Describe the morphology of the erythrocytes.
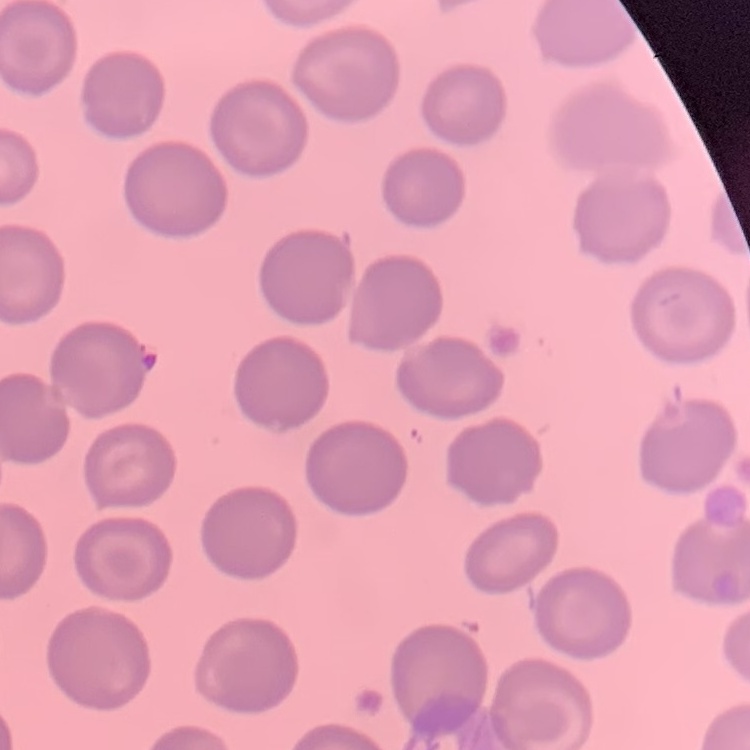
They show no rouleaux formation.

Summary:
  - Image type: one tile cut from a larger photomicrograph
  - Stain: Field's or Giemsa
  - Preparation: thin blood smear